Report the malaria status of this cell.
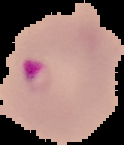
Parasitized.

Segmented cell region on a black background. From a thin blood smear. Image is 124×145 pixels.